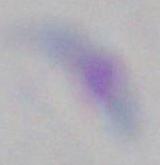
{
  "magnification": "1000x",
  "modality": "photomicrograph",
  "identification": "Toxoplasma gondii"
}